Identify the parasite.
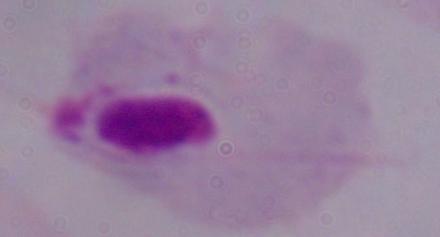
This is a trichomonad.

Summary:
  - Modality: photomicrograph
  - Magnification: 1000x